State which parasite is depicted.
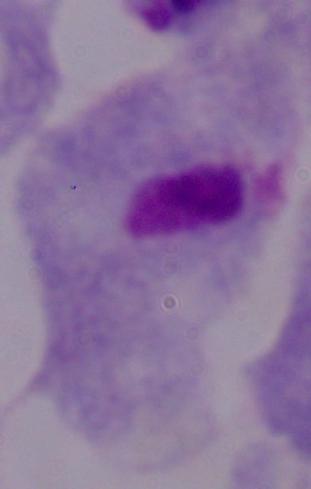
This is a trichomonad.

1000x magnification. Photomicrograph.